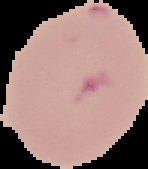
Summary:
  - Preparation: thin blood smear
  - Result: malaria parasites identified
  - Image size: 148×169 pixels
  - Image type: segmented cell region with the area outside set to black